Assess this cell for malaria.
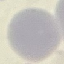
It is uninfected.

Giemsa-stained preparation. Cell patch, automatically extracted from a larger field of view and resized to 64 × 64 pixels. Photographed with a smartphone camera at the microscope eyepiece. Thin smear of blood.